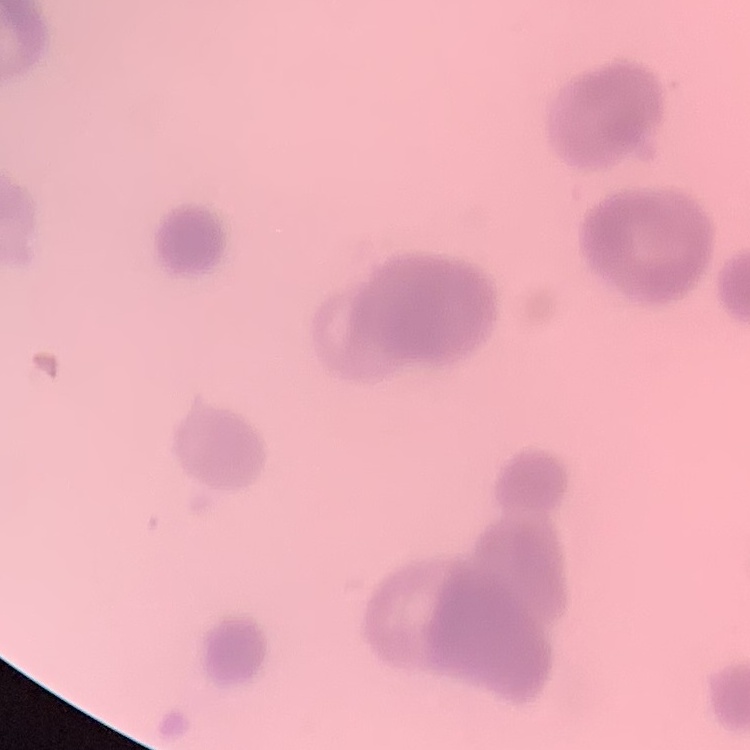
red blood cell morphology = rouleaux formation
image type = one tile cut from a larger photomicrograph
preparation = thin blood film
stain = Field's or Giemsa